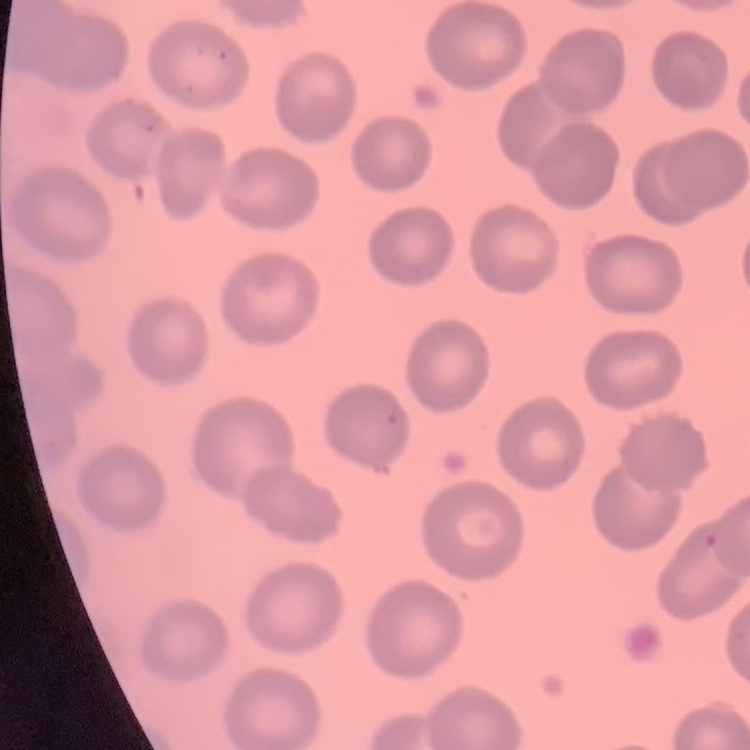
red blood cell morphology = no rouleaux formation
stain = Field's or Giemsa
preparation = thin blood film
image type = one tile cut from a larger photomicrograph